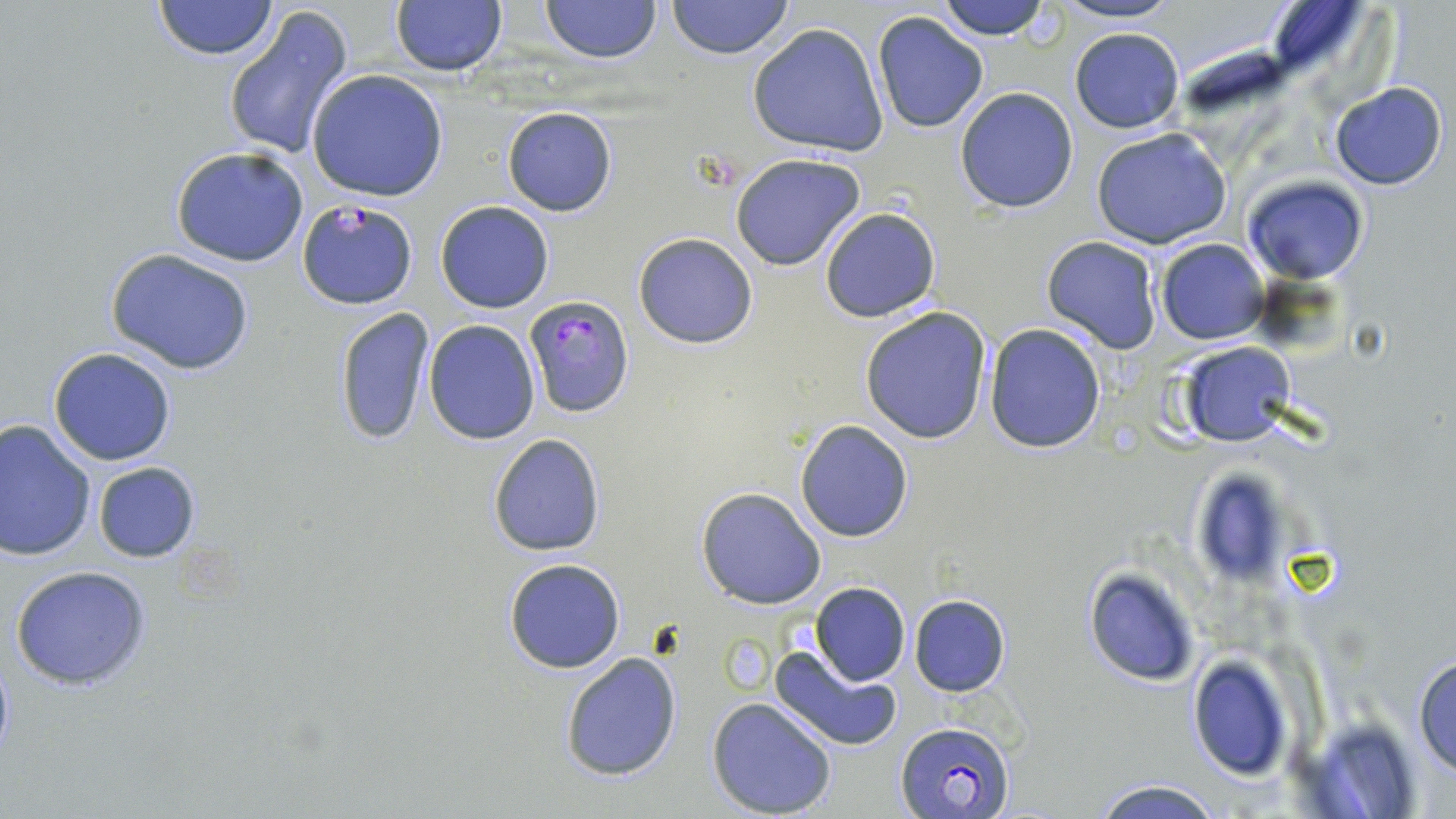

slide_level_diagnosis: Plasmodium falciparum
preparation: thin blood film
plasmodium_falciparum_infected_red_blood_cell_locations: 'approximate bounding boxes as (x1,y1)-(x2,y2) corner pairs in pixels: (296,198)-(418,310), (522,294)-(636,419), (892,718)-(1015,819)'
field_of_view: single
modality: optical microscopy
magnification: 1000x
image_size: 1456×819 pixels
stain: May-Grünwald-Giemsa
uninfected_red_blood_cell_locations: 'approximate bounding boxes as (x1,y1)-(x2,y2) corner pairs in pixels: (153,0)-(276,60), (540,0)-(659,62), (665,0)-(795,58), (933,0)-(1052,41), (1050,0)-(1186,26), (388,1)-(507,77), (223,5)-(355,159), (871,9)-(990,134), (747,22)-(888,158), (1068,26)-(1186,133), (307,70)-(449,201), (1330,83)-(1448,189), (953,87)-(1078,213), (502,106)-(617,217), (1090,129)-(1233,248), (171,145)-(310,267), (730,153)-(865,271), (1245,174)-(1367,285), (435,201)-(555,313), (819,206)-(941,322), (634,233)-(757,349), (1041,236)-(1162,354), (1155,239)-(1268,344), (106,248)-(257,374), (860,306)-(992,445), (334,307)-(435,448), (423,319)-(539,444), (984,324)-(1107,452), (1179,342)-(1296,447), (47,347)-(177,466), (0,418)-(97,561), (794,421)-(913,541), (487,433)-(605,557), (92,461)-(201,563), (1188,471)-(1291,589), (695,487)-(826,610), (503,559)-(627,674), (8,564)-(154,691), (1083,567)-(1202,687), (811,582)-(910,686), (909,595)-(1012,697), (769,642)-(903,753), (559,650)-(684,783), (1412,650)-(1456,777), (1186,655)-(1293,780), (707,697)-(837,819), (1087,778)-(1225,818)'